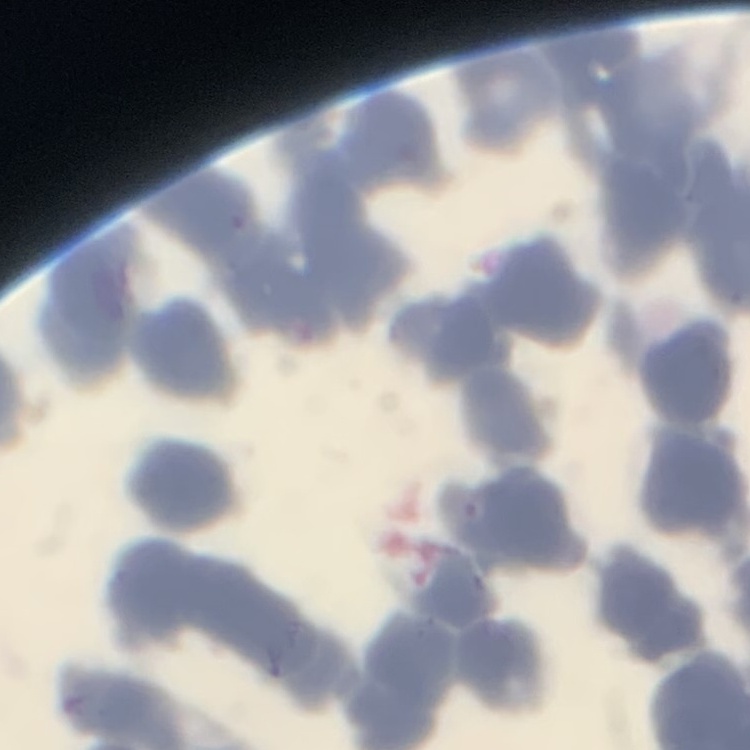

The red blood cells show rouleaux formation. Field's or Giemsa stain. Thin blood film. One tile cut from a larger photomicrograph.